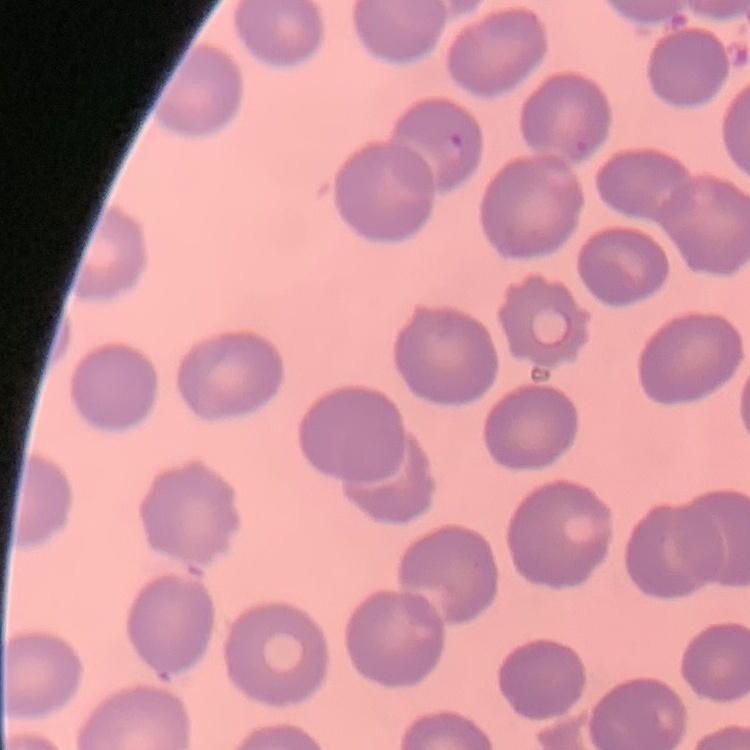
erythrocyte morphology = no rouleaux formation
stain = Field's or Giemsa
image type = one tile cut from a larger photomicrograph
preparation = thin blood smear